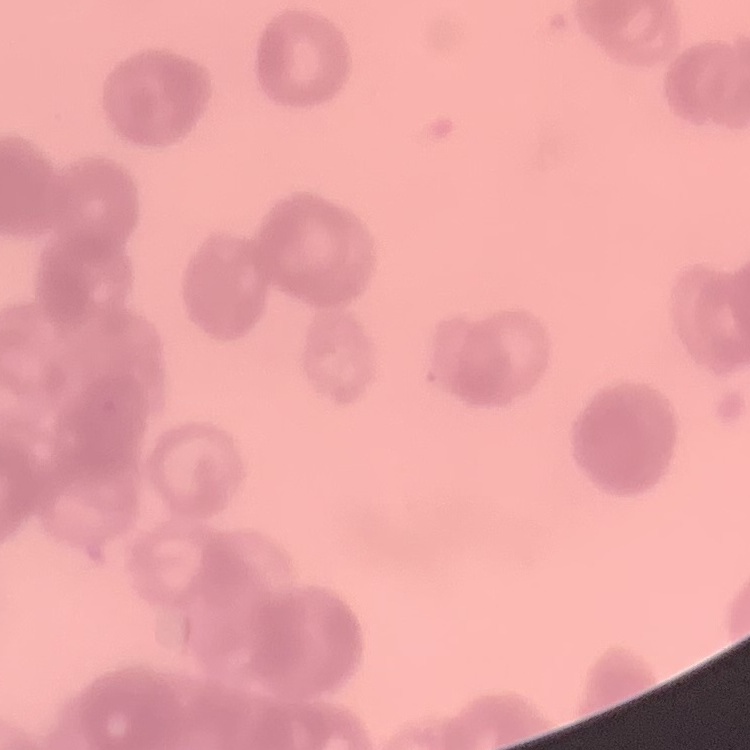
red_blood_cell_morphology: rouleaux formation
image_type: one tile cut from a larger photomicrograph
stain: Field's or Giemsa
preparation: thin peripheral smear